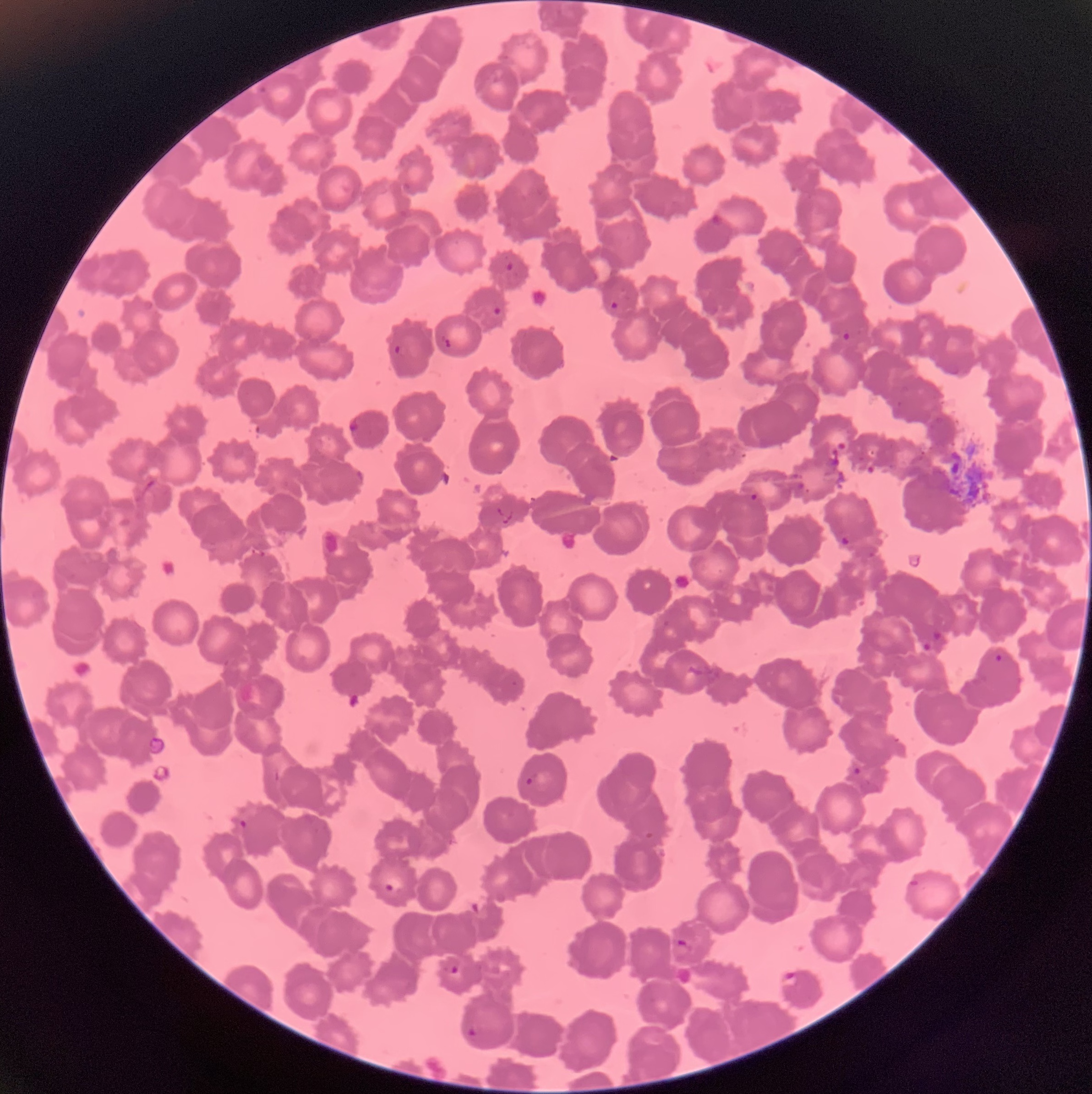
Summary:
  - Coordinate format: approximate bounding boxes as (x1, y1, x2, y2) in pixels
  - Plasmodium parasite locations: (710, 212, 724, 225), (504, 261, 514, 272), (609, 300, 619, 315), (491, 306, 503, 316), (842, 332, 851, 341), (438, 336, 453, 351), (394, 344, 408, 357), (347, 418, 361, 434), (749, 492, 758, 501), (839, 533, 850, 547), (931, 630, 942, 640), (922, 642, 931, 652), (994, 653, 1004, 664), (852, 766, 862, 776), (524, 774, 538, 788), (239, 819, 247, 828), (382, 876, 405, 895), (908, 878, 922, 891), (675, 938, 689, 948), (449, 964, 460, 976), (780, 970, 801, 988), (466, 1026, 480, 1039)
  - Image size: 1092×1094 pixels
  - Modality: optical microscopy
  - Preparation: thin blood smear
  - Red blood cell morphology: rouleaux formation